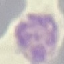
result = malaria parasites detected
preparation = thin smear
capture = smartphone through the microscope eyepiece
image type = cell patch, automatically extracted from a larger field of view and resized to 64 × 64 pixels
stain = Giemsa